Classify this cell by malaria status.
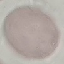

It is uninfected.

Cell patch, automatically extracted from a larger field of view and resized to 64 × 64 pixels. Acquired by smartphone through the microscope eyepiece. Giemsa-stained preparation. Thin blood film.